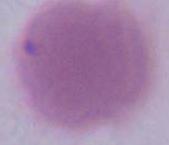

Captured at 1000x magnification. An erythrocyte is seen. Photomicrograph.